Name the parasite shown.
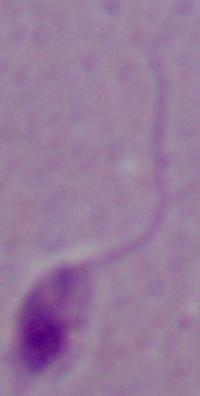

Leishmania.

Summary:
  - Magnification: 1000x
  - Modality: micrograph